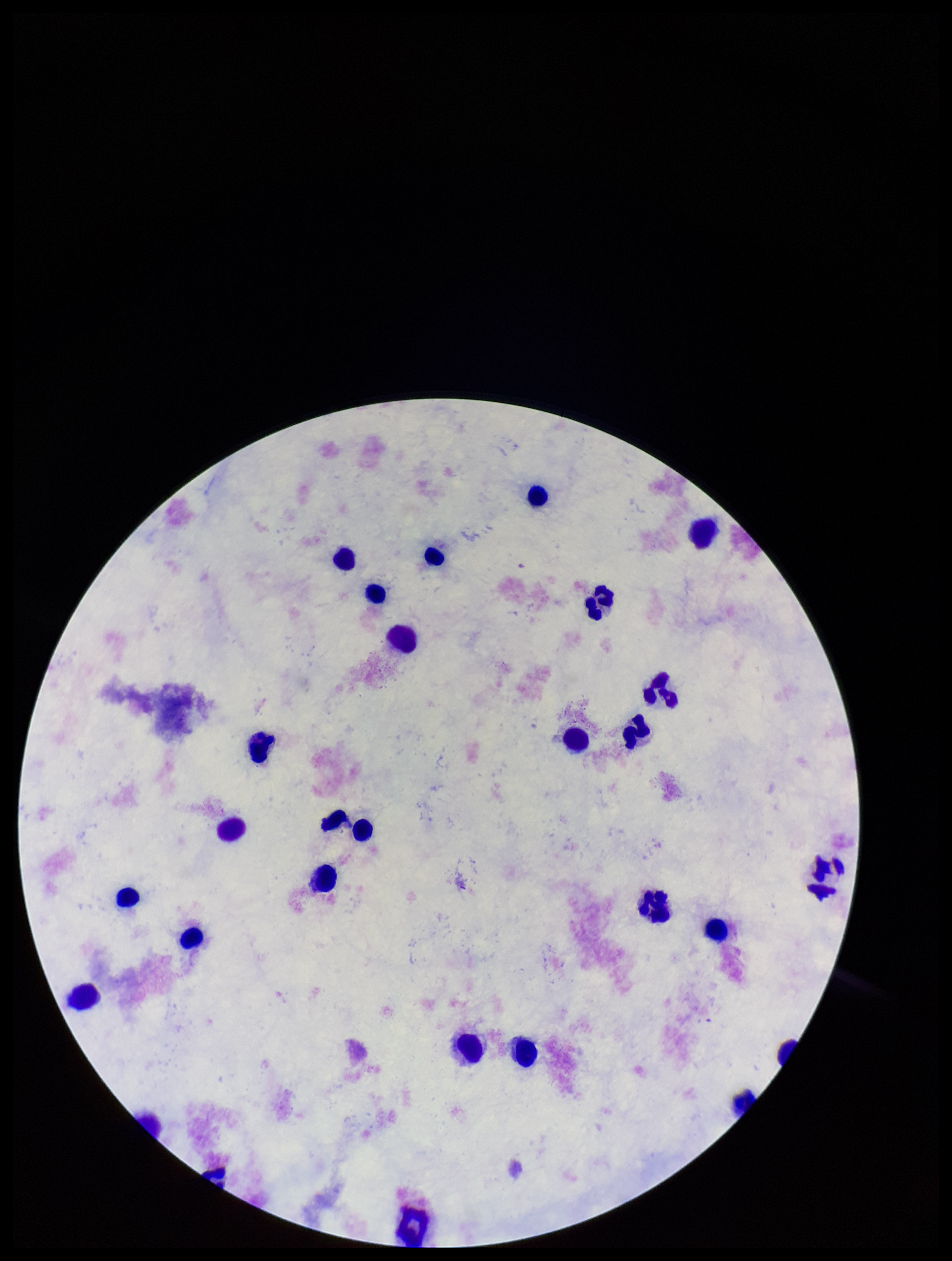
image size = 952×1261 pixels
capture = smartphone photograph through the microscope eyepiece
parasite count = 0
stain = Giemsa
leukocyte count = 27
field of view = single
preparation = thick smear
patient malaria status = negative
Plasmodium parasites = none detected